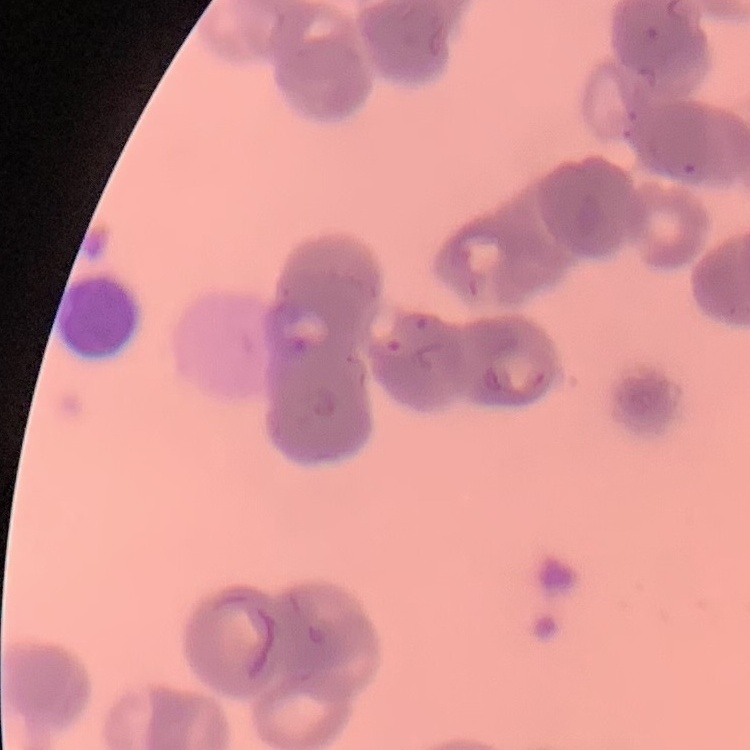

red blood cell morphology = rouleaux formation
image type = one tile cut from a larger photomicrograph
stain = Field's or Giemsa
preparation = thin peripheral smear